Name the cell type shown.
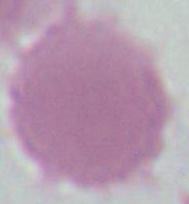

An erythrocyte.

{
  "magnification": "1000x",
  "modality": "photomicrograph"
}